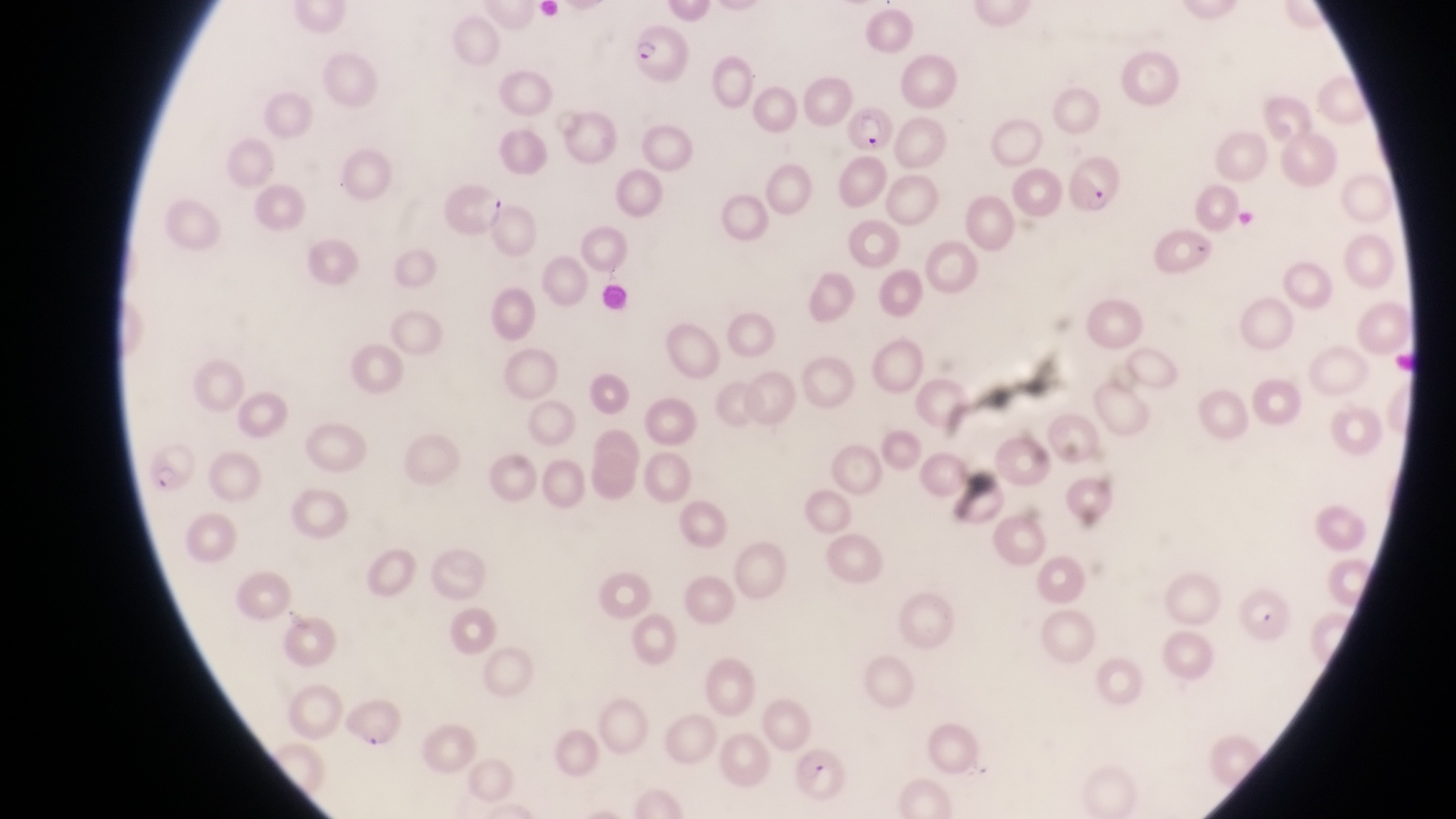 Approximate bounding boxes as {left, top, right, bottom} in pixels. Parasitised red blood cell locations: {629, 30, 688, 89}, {843, 109, 898, 156}, {1065, 161, 1128, 222}, {436, 182, 507, 238}, {145, 444, 195, 491}, {1241, 585, 1296, 643}, {336, 698, 405, 753}, {793, 746, 846, 798}. Thin blood film. Magnification of 1000x. Single field of view. Sample from Uganda. Image is 1456×819 pixels. Captured by a smartphone held over the eyepiece of an Olympus CX-23 microscope.